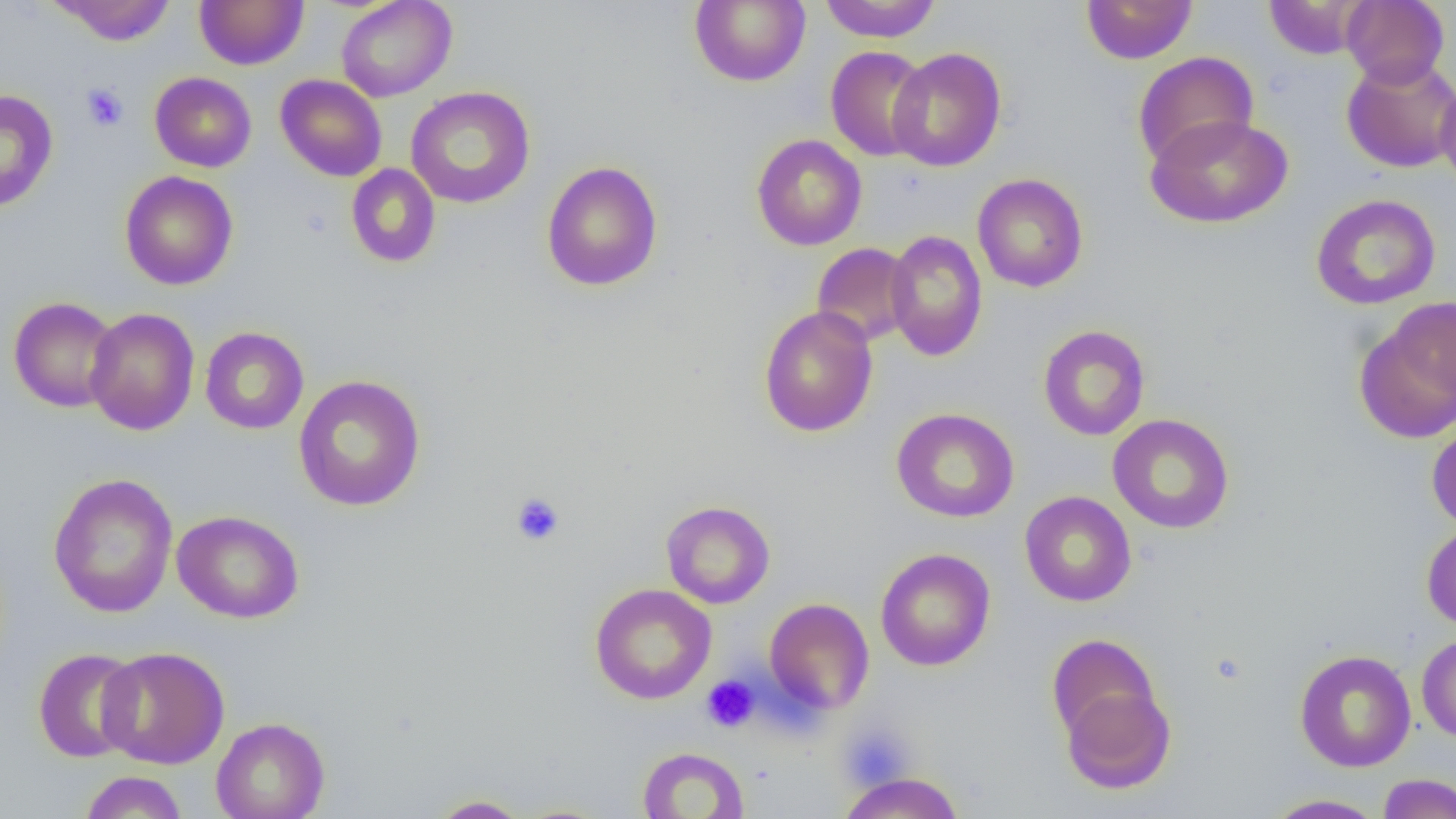
Approximate bounding boxes as (x1, y1, x2, y2) in pixels. Uninfected red blood cell locations: (195, 0, 308, 69), (336, 0, 456, 102), (689, 0, 810, 87), (818, 0, 943, 43), (1081, 0, 1198, 65), (1341, 0, 1449, 87), (50, 1, 177, 45), (1263, 1, 1371, 59), (825, 45, 932, 162), (887, 47, 1006, 171), (1133, 52, 1259, 169), (1341, 55, 1456, 173), (150, 72, 257, 173), (275, 74, 387, 182), (1435, 75, 1456, 194), (406, 86, 536, 208), (0, 89, 58, 211), (1145, 114, 1293, 229), (751, 134, 867, 251), (541, 161, 663, 292), (345, 163, 440, 268), (119, 171, 238, 290), (972, 173, 1088, 293), (1311, 193, 1441, 310), (884, 229, 988, 361), (812, 242, 916, 346), (8, 296, 122, 413), (1356, 301, 1455, 444), (758, 306, 878, 437), (84, 307, 200, 435), (1038, 324, 1151, 441), (199, 326, 309, 434), (294, 375, 426, 511), (891, 407, 1019, 523), (1107, 413, 1235, 534), (1426, 420, 1456, 531), (47, 473, 178, 618), (1020, 491, 1137, 607), (661, 501, 775, 609), (172, 509, 304, 624), (1421, 522, 1456, 631), (875, 548, 996, 671), (590, 583, 716, 705), (764, 598, 874, 714), (1046, 633, 1163, 748), (1416, 633, 1456, 743), (97, 646, 230, 769), (32, 647, 144, 763), (1294, 649, 1416, 772), (1059, 678, 1175, 794), (211, 716, 329, 819), (637, 746, 749, 819), (79, 771, 188, 818), (836, 771, 964, 819), (1377, 773, 1456, 818), (427, 794, 531, 818), (1264, 794, 1387, 818). Platelet locations: (81, 83, 129, 132), (511, 493, 565, 546), (700, 674, 760, 733), (836, 722, 918, 792). Slide-level diagnosis: no evidence of blood parasites. Single field of view. Image is 1456×819 pixels. Captured at 1000x magnification. Thin blood film. Optical microscopy.